Locate and identify every blood parasite.
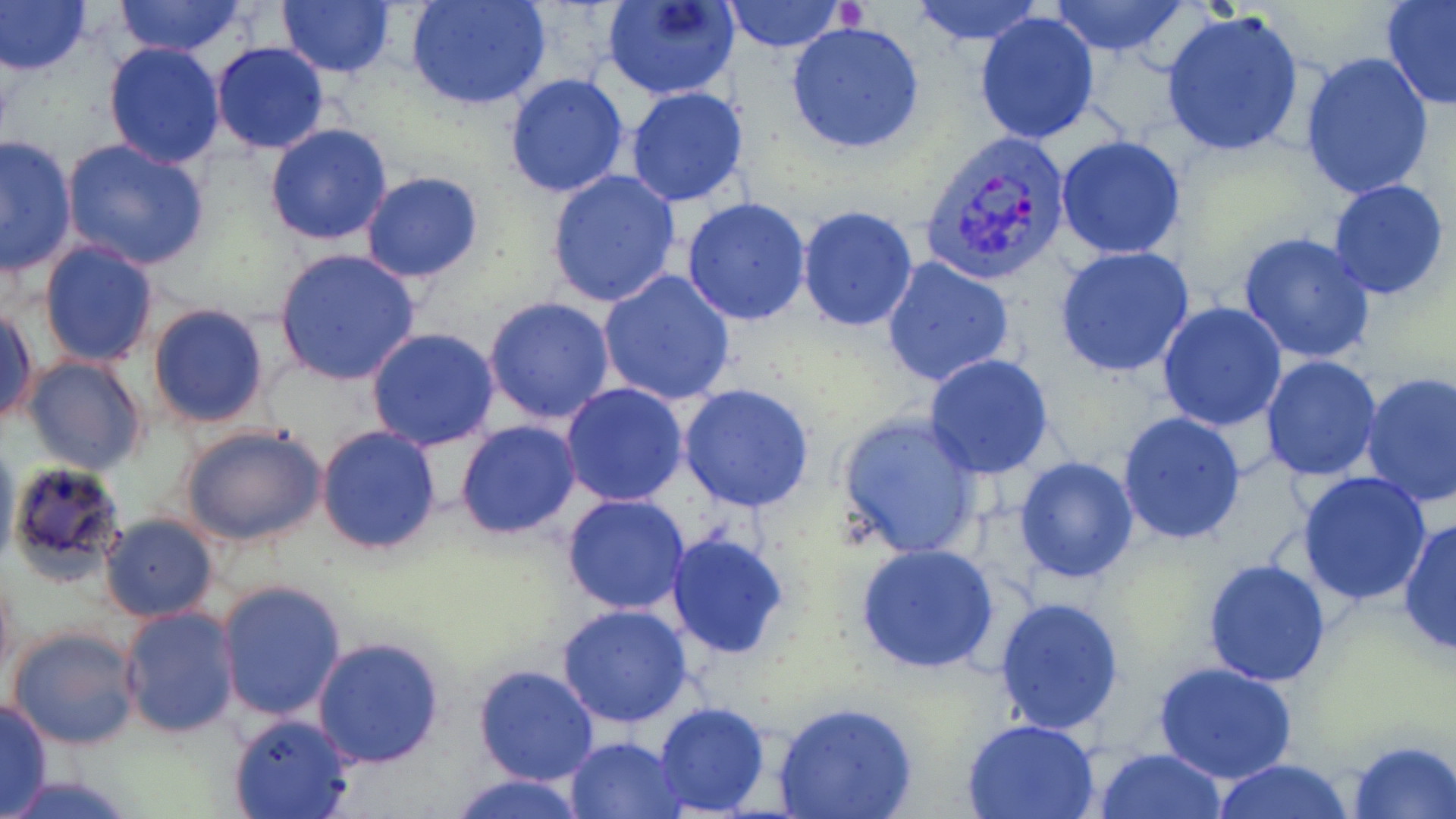

Approximate bounding boxes as (x1, y1, x2, y2) in pixels.
Plasmodium vivax-infected red blood cells: (922, 131, 1073, 285).
No Plasmodium falciparum, Plasmodium ovale, Plasmodium malariae, Babesia divergens, or Trypanosoma brucei observed.

Platelet locations: (840, 0, 866, 29). Uninfected red blood cell locations: (0, 0, 92, 77), (277, 0, 398, 79), (406, 0, 552, 110), (604, 0, 741, 101), (906, 0, 1047, 47), (1048, 0, 1188, 57), (1380, 0, 1456, 110), (111, 1, 249, 57), (721, 1, 849, 53), (1161, 6, 1306, 159), (974, 9, 1102, 145), (786, 20, 927, 155), (103, 42, 227, 169), (210, 42, 329, 154), (1298, 51, 1435, 201), (503, 73, 630, 199), (625, 86, 748, 208), (264, 123, 394, 245), (1, 135, 76, 277), (1057, 135, 1185, 260), (59, 139, 210, 270), (544, 167, 681, 309), (359, 171, 484, 283), (1327, 179, 1450, 301), (680, 197, 812, 324), (796, 206, 920, 332), (1236, 231, 1378, 365), (38, 239, 161, 370), (1054, 246, 1196, 379), (273, 248, 422, 386), (880, 257, 1018, 391), (596, 269, 738, 408), (484, 297, 616, 424), (1157, 300, 1289, 432), (1, 303, 37, 427), (147, 303, 270, 429), (367, 327, 500, 450), (21, 354, 150, 476), (923, 354, 1056, 480), (1260, 355, 1383, 483), (1359, 372, 1456, 508), (560, 382, 690, 506), (678, 382, 815, 512), (1116, 410, 1247, 545), (838, 412, 985, 559), (455, 419, 582, 538), (178, 421, 328, 550), (315, 425, 442, 556), (0, 435, 18, 570), (1013, 455, 1139, 584), (6, 459, 128, 590), (1297, 471, 1434, 606), (561, 493, 691, 614), (99, 513, 219, 623), (1397, 516, 1456, 659), (666, 533, 792, 659), (855, 543, 1001, 675), (1202, 558, 1330, 686), (0, 565, 16, 689), (217, 581, 348, 722), (992, 596, 1125, 737), (555, 605, 695, 729), (117, 606, 238, 739), (6, 626, 141, 752), (312, 636, 446, 768), (1153, 661, 1298, 786), (474, 664, 598, 787), (0, 698, 52, 818), (771, 700, 917, 819), (652, 703, 772, 817), (227, 714, 353, 819), (961, 718, 1102, 818), (566, 736, 688, 819), (1347, 739, 1455, 819), (1094, 748, 1228, 819), (1211, 759, 1358, 818), (2, 772, 144, 819), (449, 772, 588, 819). Slide-level diagnosis: Plasmodium vivax. May-Grünwald-Giemsa stain. 1000x magnification. Optical microscopy. Thin blood film. Image is 1456×819 pixels. One field of a larger specimen.